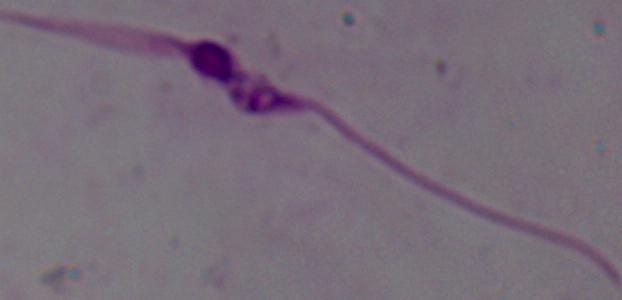

Summary:
  - Identification: Leishmania
  - Modality: photomicrograph
  - Magnification: 1000x